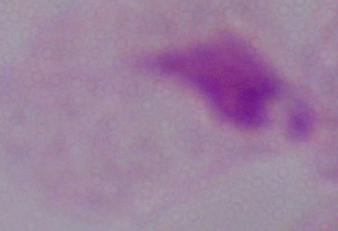

modality: micrograph
identification: trichomonad
magnification: 1000x